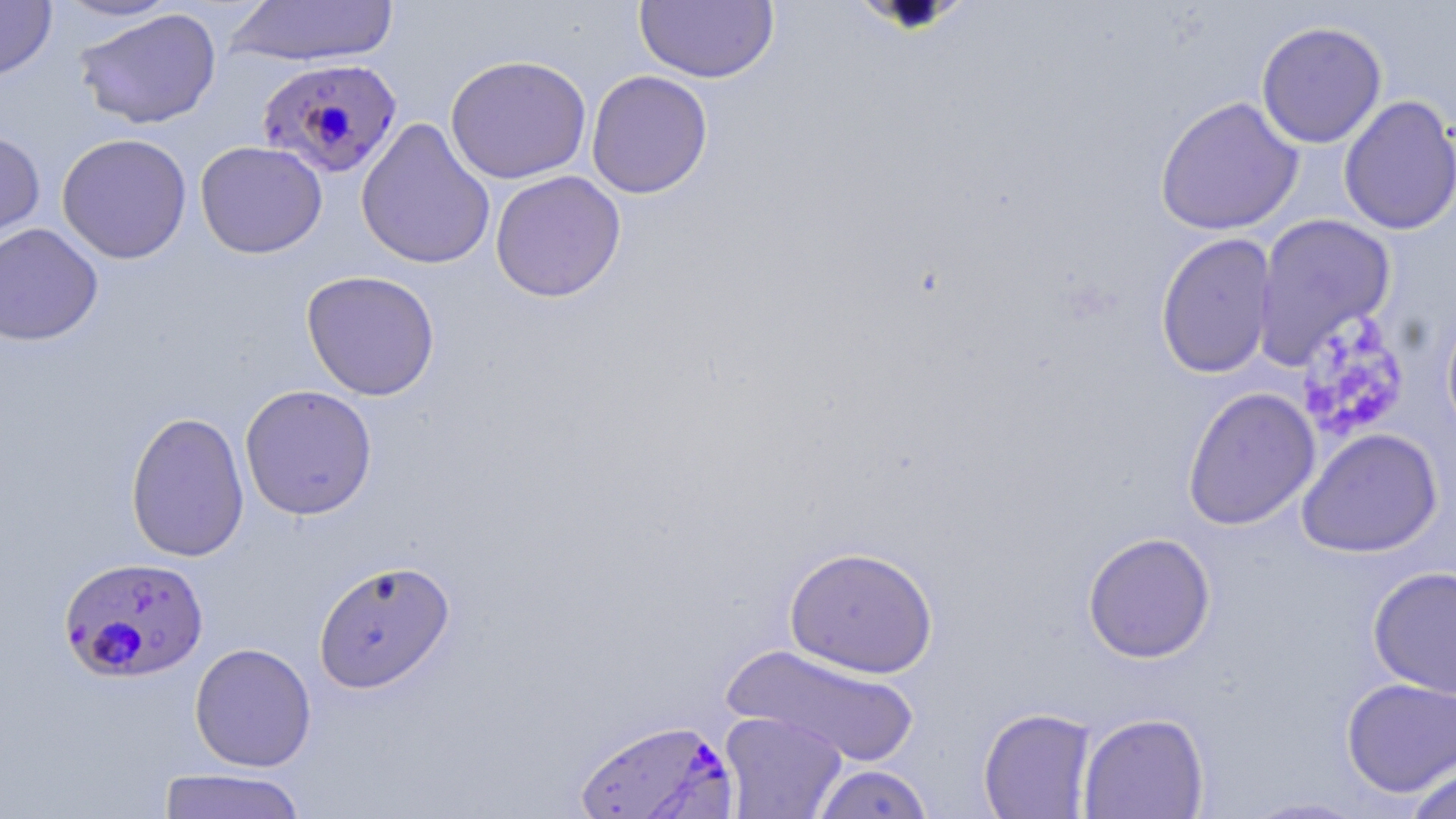
Approximate bounding boxes as named x1/y1/x2/y2 corners in pixels. Plasmodium falciparum-infected red blood cell locations: (x1=257, y1=57, x2=403, y2=179), (x1=59, y1=556, x2=208, y2=684), (x1=573, y1=717, x2=740, y2=818). Uninfected red blood cell locations: (x1=0, y1=0, x2=57, y2=81), (x1=52, y1=0, x2=183, y2=22), (x1=228, y1=0, x2=400, y2=68), (x1=633, y1=1, x2=780, y2=84), (x1=74, y1=8, x2=222, y2=130), (x1=1256, y1=21, x2=1387, y2=149), (x1=444, y1=54, x2=592, y2=185), (x1=585, y1=70, x2=713, y2=199), (x1=1338, y1=95, x2=1456, y2=237), (x1=1154, y1=96, x2=1304, y2=236), (x1=356, y1=117, x2=496, y2=271), (x1=0, y1=130, x2=46, y2=250), (x1=56, y1=133, x2=193, y2=264), (x1=195, y1=141, x2=328, y2=259), (x1=489, y1=170, x2=627, y2=303), (x1=1252, y1=212, x2=1396, y2=370), (x1=0, y1=222, x2=104, y2=346), (x1=1155, y1=232, x2=1277, y2=379), (x1=301, y1=270, x2=440, y2=401), (x1=1441, y1=301, x2=1456, y2=445), (x1=239, y1=384, x2=378, y2=520), (x1=1182, y1=387, x2=1321, y2=530), (x1=125, y1=410, x2=250, y2=563), (x1=1296, y1=429, x2=1443, y2=557), (x1=1082, y1=532, x2=1217, y2=663), (x1=784, y1=545, x2=940, y2=679), (x1=313, y1=559, x2=456, y2=695), (x1=1367, y1=566, x2=1456, y2=700), (x1=189, y1=642, x2=317, y2=772), (x1=723, y1=644, x2=921, y2=765), (x1=1340, y1=677, x2=1456, y2=797), (x1=978, y1=707, x2=1096, y2=818), (x1=719, y1=711, x2=847, y2=819), (x1=1077, y1=712, x2=1210, y2=818), (x1=1404, y1=760, x2=1456, y2=819), (x1=809, y1=763, x2=935, y2=818), (x1=157, y1=768, x2=309, y2=818), (x1=1237, y1=796, x2=1373, y2=818). Platelet locations: (x1=1295, y1=313, x2=1411, y2=442). Slide-level diagnosis: Plasmodium falciparum. One field of a larger specimen. May-Grünwald-Giemsa-stained preparation. Thin blood smear. Captured at 1000x magnification. Optical microscopy. Image is 1456×819 pixels.